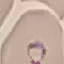
Malaria status: parasitized. Acquired by smartphone through the microscope eyepiece. Automatically extracted cell patch, resized to 64 × 64 pixels. Giemsa-stained preparation. Thin blood film.